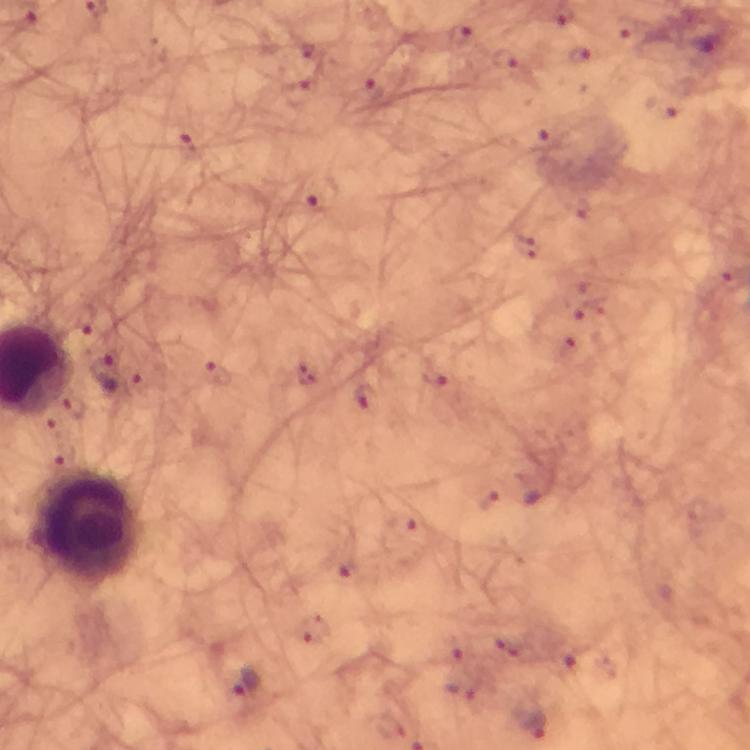
context = from a diagnostic examination for malaria
magnification = 100x
cropped from = one field of view
Plasmodium parasite locations = approximate object centers, in pixels from the top-left corner: (x=322, y=198), (x=217, y=372), (x=108, y=373), (x=363, y=397), (x=246, y=684), (x=532, y=726)
stain = Giemsa
preparation = thick blood film
immersion oil = applied
leukocyte locations = approximate object centers, in pixels from the top-left corner: (x=89, y=524)
capture = smartphone mounted on the microscope
image size = 750×750 pixels